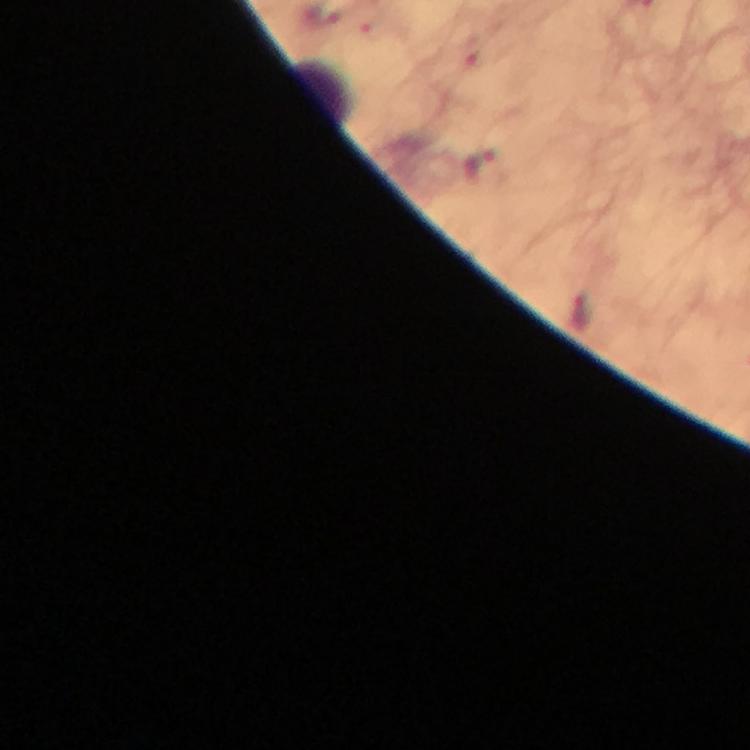 Approximate centers as (x, y) in pixels. Leukocyte locations: (320, 93). Malaria parasite locations: (479, 166), (584, 315). 100x magnification. From a malaria diagnostic workup. Cropped region of a single field of view. Thick blood film. Image is 750×750 pixels. Giemsa-stained preparation. Immersion oil was used. Smartphone photograph taken through a microscope.